Report the malaria status of this cell.
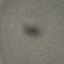
It is uninfected.

Acquired by smartphone through the microscope eyepiece. Thin blood smear. Cell patch, automatically extracted from a larger field of view and resized to 64 × 64 pixels. Giemsa stain.